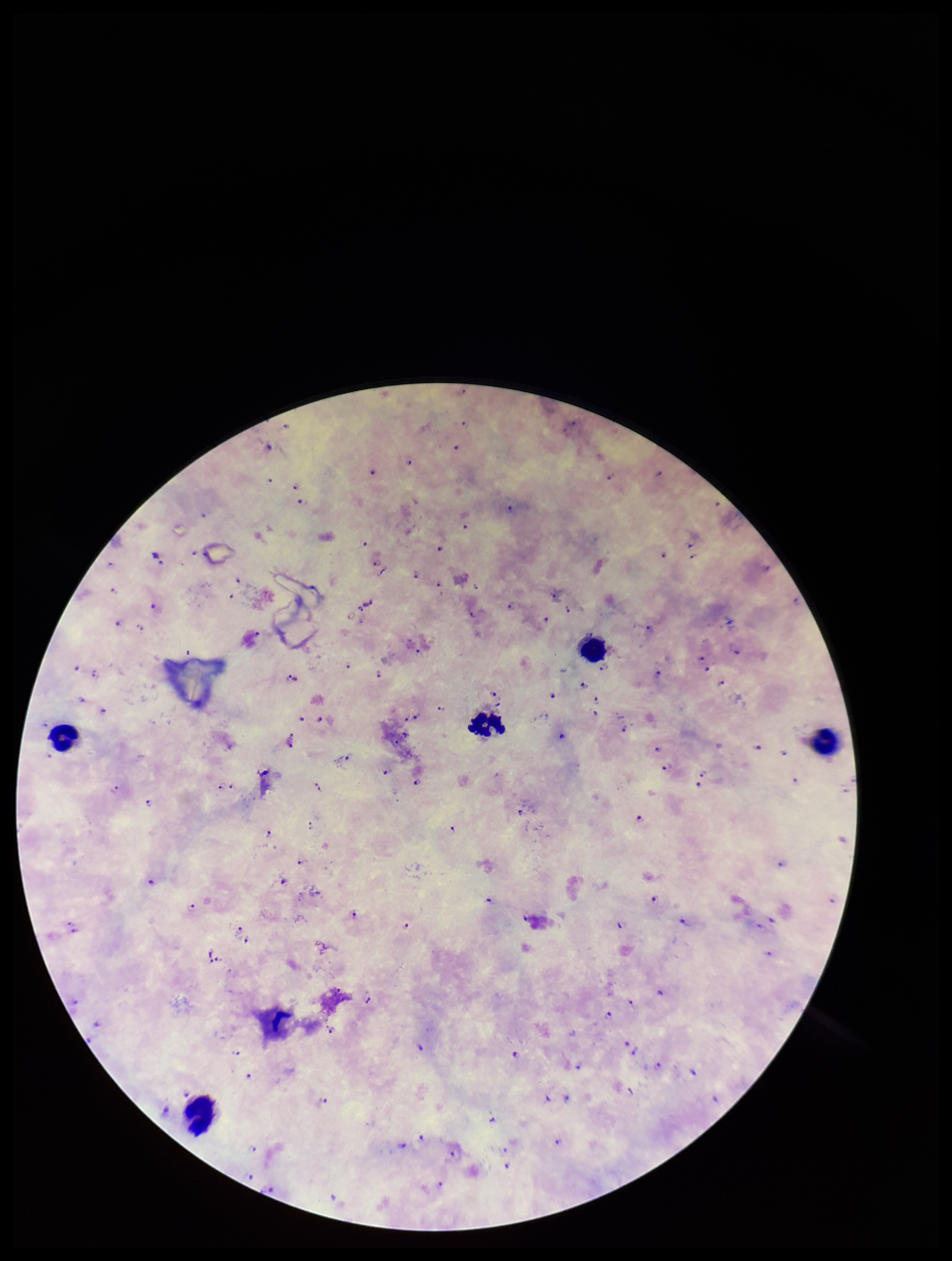

leukocyte count = 5
parasite count = 88
preparation = thick smear
Plasmodium parasites = detected
stain = Giemsa
field of view = one from this slide
patient malaria status = positive
image size = 952×1261 pixels
capture = smartphone photograph through the microscope eyepiece
species reported for this patient = Plasmodium falciparum